Name the parasite shown.
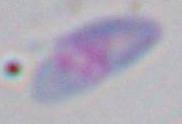

Toxoplasma gondii.

modality: micrograph
magnification: 1000x